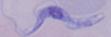
Micrograph. A trypanosome is shown. 1000x magnification.